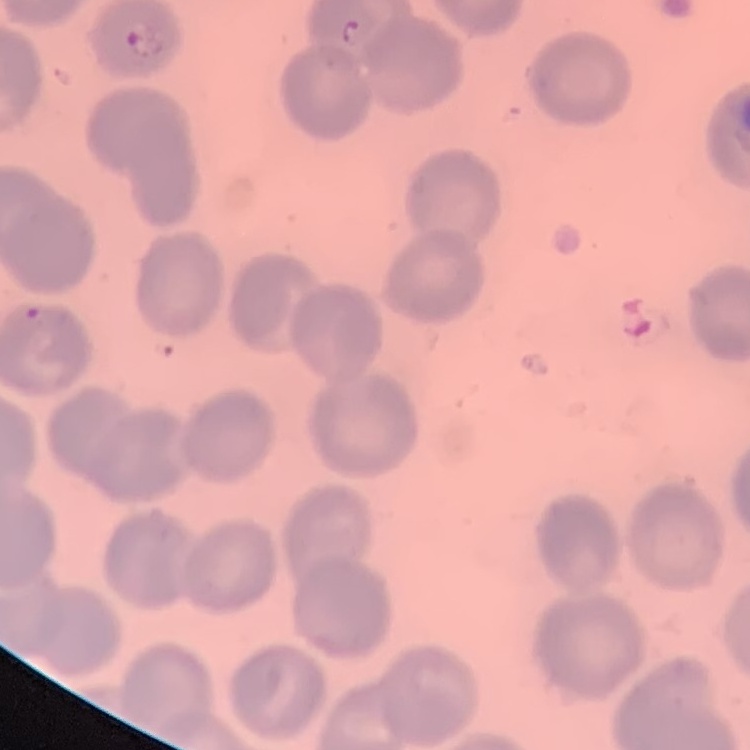 The erythrocytes show no rouleaux formation. Thin blood smear. Stained with either Field's or Giemsa. Square crop of a larger photomicrograph.